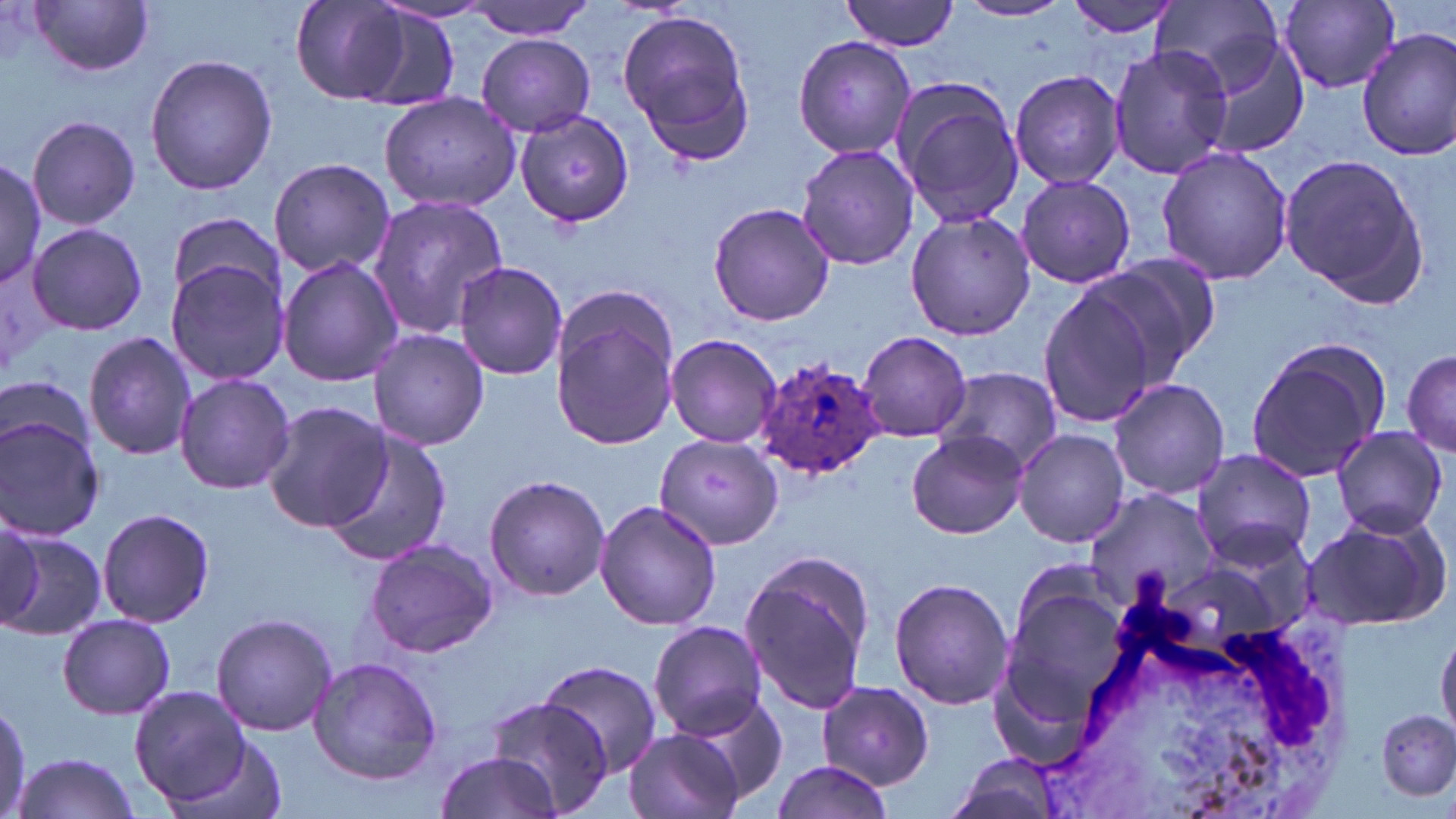
Summary:
  - Coordinate format: approximate bounding boxes as (x1,y1)-(x2,y2) corner pairs in pixels
  - Plasmodium ovale-infected red blood cell locations: (754,357)-(885,477)
  - Uninfected red blood cell locations: (30,0)-(156,77), (287,0)-(415,105), (467,0)-(595,40), (842,0)-(960,52), (1060,0)-(1182,38), (1152,0)-(1280,90), (1279,1)-(1401,92), (954,2)-(1073,23), (347,6)-(463,112), (616,9)-(759,161), (1201,27)-(1312,158), (1356,28)-(1456,159), (477,34)-(595,136), (793,34)-(916,161), (1107,45)-(1234,180), (144,55)-(277,196), (1008,68)-(1126,189), (891,80)-(1025,231), (379,92)-(520,211), (515,110)-(635,228), (25,115)-(141,232), (796,141)-(920,272), (1156,144)-(1293,286), (1277,150)-(1431,308), (268,157)-(397,279), (0,158)-(45,285), (1014,176)-(1137,288), (367,196)-(511,336), (706,201)-(836,327), (904,208)-(1035,342), (165,213)-(282,311), (26,222)-(147,336), (1090,252)-(1226,379), (277,255)-(406,388), (163,259)-(289,387), (453,260)-(569,382), (1036,282)-(1165,431), (547,286)-(683,452), (369,327)-(488,451), (857,330)-(972,442), (83,331)-(196,461), (663,333)-(783,449), (1244,338)-(1390,480), (1400,346)-(1455,459), (934,368)-(1062,478), (174,373)-(296,495), (1107,379)-(1231,500), (260,401)-(391,534), (0,414)-(105,540), (322,426)-(452,564), (1330,426)-(1448,536), (1014,428)-(1131,548), (905,431)-(1026,539), (656,433)-(782,548), (1193,448)-(1317,566), (484,474)-(611,601), (1084,485)-(1218,607), (593,498)-(724,631), (97,506)-(217,627), (1300,510)-(1453,631), (0,531)-(105,640), (363,536)-(499,660), (738,547)-(875,715), (889,577)-(1015,710), (1000,585)-(1133,723), (211,612)-(336,738), (57,613)-(176,719), (646,621)-(771,741), (1437,630)-(1456,738), (306,656)-(444,785), (538,659)-(662,778), (816,681)-(936,790), (130,687)-(254,807), (678,694)-(789,806), (485,697)-(615,818), (1376,708)-(1456,799), (625,729)-(744,819), (162,734)-(294,819), (432,751)-(561,819), (12,753)-(143,819), (943,754)-(1068,819), (771,759)-(894,819)
  - White blood cell locations: (1035,558)-(1354,819)
  - Slide-level diagnosis: Plasmodium ovale
  - Preparation: thin blood smear
  - Field of view: single
  - Image size: 1456×819 pixels
  - Stain: May-Grünwald-Giemsa
  - Magnification: 1000x
  - Modality: light microscopy